Give the position of every Plasmodium parasite visible.
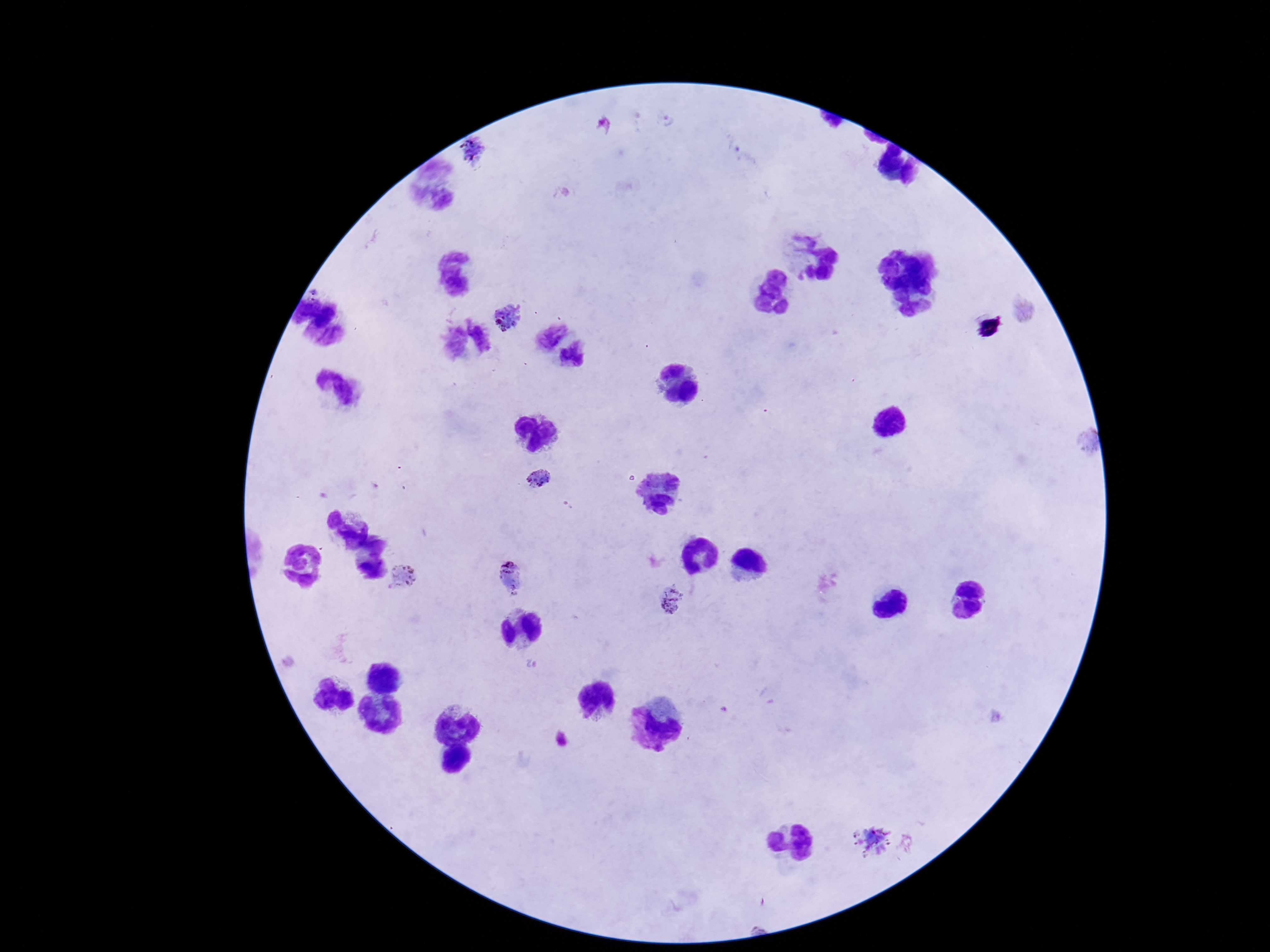

Approximate object centers, in pixels from the top-left corner.
Plasmodium parasites: (x=470, y=149), (x=510, y=321), (x=538, y=479), (x=509, y=575), (x=404, y=578), (x=672, y=600), (x=871, y=841).

Summary:
  - Stain: Giemsa
  - Magnification: 100x
  - Patient malaria status: infected
  - Preparation: thick blood film
  - Image size: 1270×952 pixels
  - Capture: smartphone camera through the microscope eyepiece
  - Field of view: one from this slide